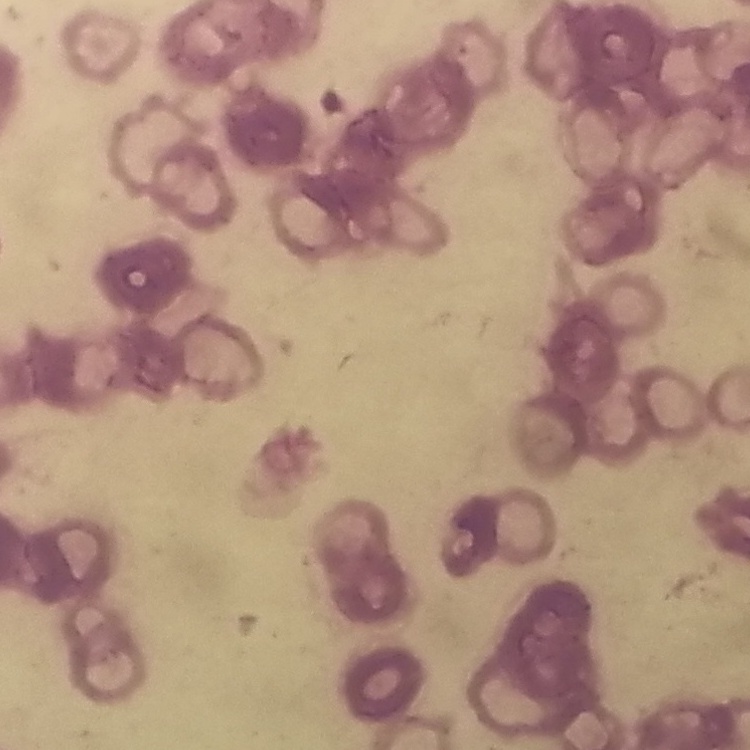

Summary:
  - Erythrocyte morphology: rouleaux formation
  - Image type: square crop of a larger photomicrograph
  - Preparation: thin blood smear
  - Stain: Field's or Giemsa